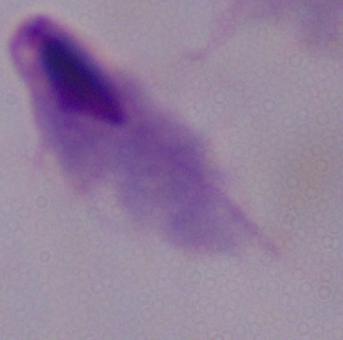
magnification: 1000x
modality: photomicrograph
identification: trichomonad